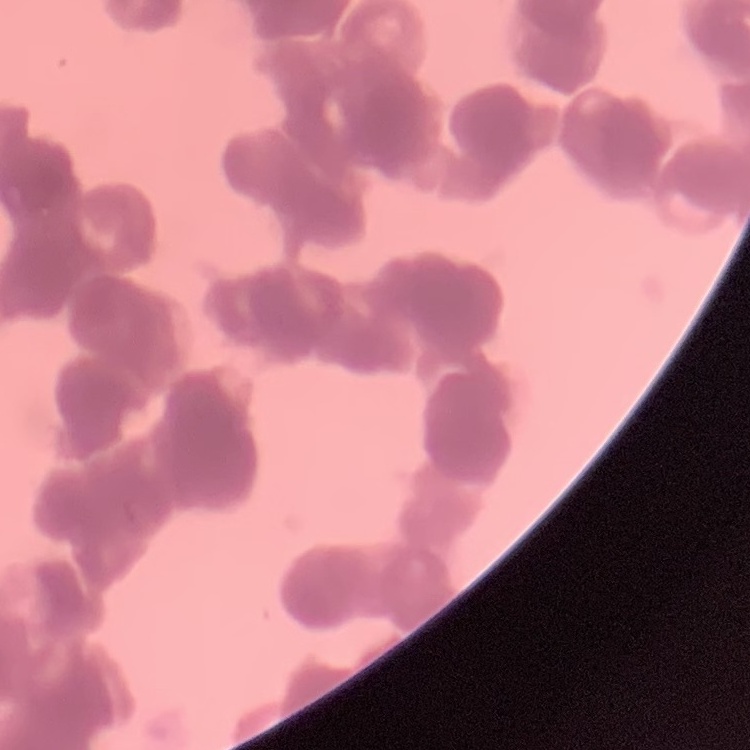
{
  "red_blood_cell_morphology": "rouleaux formation",
  "image_type": "one tile cut from a larger photomicrograph",
  "stain": "Field's or Giemsa",
  "preparation": "thin blood film"
}